Locate every cell, classifying each as a parasitized red blood cell, an uninfected red blood cell, or a white blood cell.
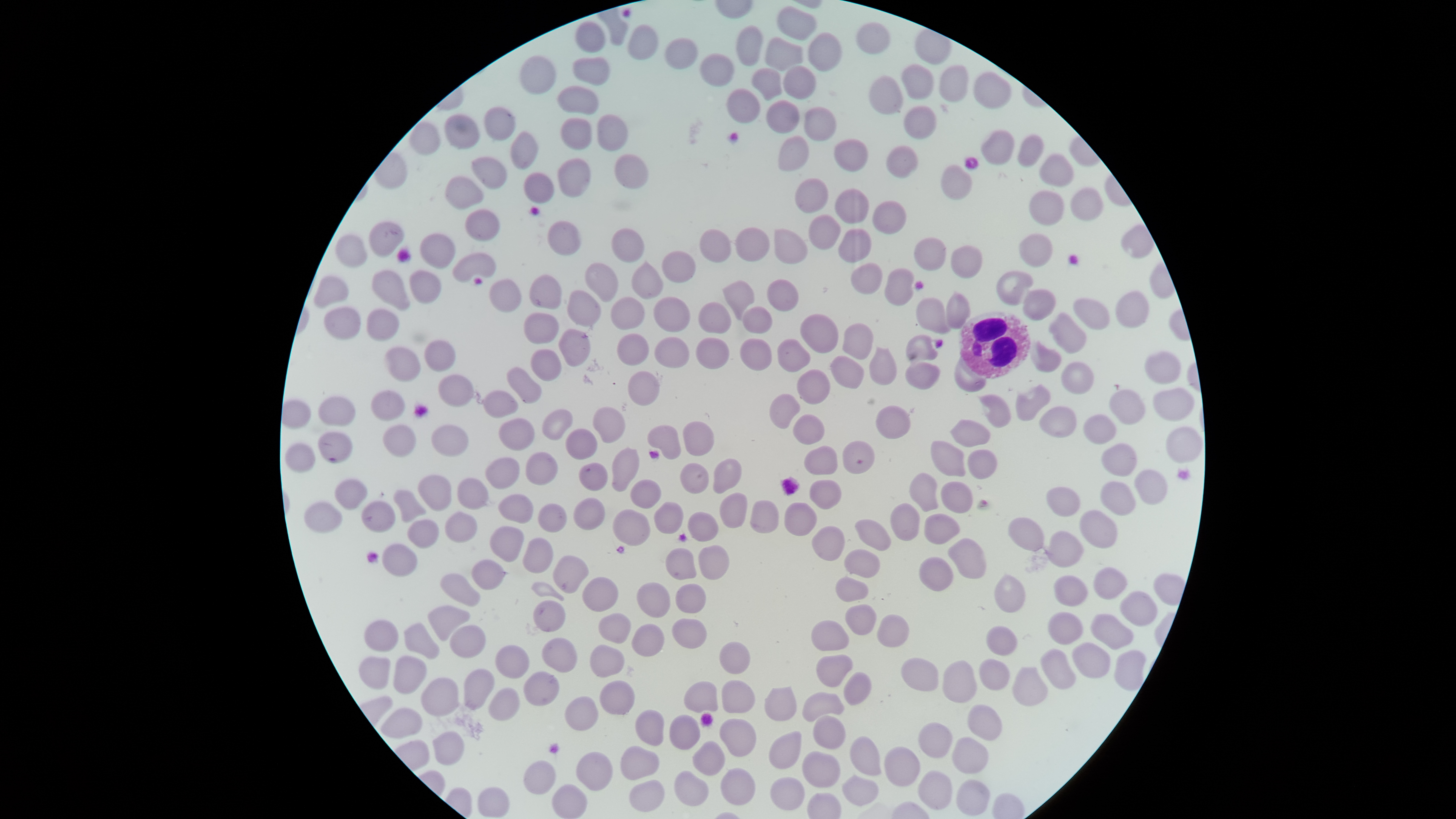

No parasitized red blood cells identified.
Approximate bounding boxes as {left, top, right, bottom} in pixels.
Uninfected red blood cells: {776, 6, 816, 40}, {574, 20, 605, 54}, {856, 22, 890, 55}, {627, 24, 658, 61}, {736, 24, 762, 66}, {808, 32, 842, 73}, {664, 37, 698, 70}, {765, 37, 803, 71}, {699, 53, 734, 88}, {520, 56, 556, 95}, {572, 56, 610, 86}, {901, 64, 934, 100}, {783, 65, 817, 99}, {939, 65, 969, 103}, {751, 68, 783, 101}, {973, 71, 1012, 109}, {868, 75, 904, 116}, {557, 86, 599, 115}, {726, 89, 760, 124}, {766, 99, 800, 134}, {903, 105, 936, 139}, {483, 106, 516, 141}, {803, 106, 837, 142}, {443, 114, 480, 150}, {597, 114, 628, 152}, {560, 118, 592, 150}, {409, 121, 440, 155}, {980, 129, 1015, 166}, {510, 130, 538, 170}, {1017, 134, 1044, 167}, {778, 135, 809, 172}, {833, 139, 869, 173}, {886, 145, 919, 179}, {1038, 153, 1075, 187}, {614, 154, 650, 189}, {471, 156, 507, 190}, {557, 159, 591, 197}, {940, 164, 973, 201}, {523, 173, 554, 204}, {445, 176, 483, 209}, {794, 178, 829, 213}, {1069, 187, 1103, 221}, {835, 188, 869, 224}, {1028, 190, 1065, 226}, {872, 200, 906, 234}, {464, 209, 500, 242}, {808, 214, 841, 250}, {547, 220, 581, 256}, {368, 221, 405, 258}, {735, 227, 770, 261}, {611, 228, 645, 263}, {838, 228, 871, 263}, {699, 229, 731, 262}, {774, 229, 808, 265}, {1018, 233, 1054, 267}, {335, 234, 367, 268}, {419, 234, 456, 269}, {913, 237, 947, 271}, {950, 245, 982, 279}, {661, 250, 697, 283}, {451, 252, 497, 283}, {630, 260, 664, 299}, {585, 263, 619, 303}, {851, 263, 883, 295}, {884, 268, 915, 306}, {371, 269, 411, 311}, {409, 270, 441, 304}, {996, 270, 1033, 307}, {529, 275, 563, 310}, {313, 276, 348, 309}, {766, 279, 799, 312}, {722, 280, 754, 320}, {1022, 288, 1056, 322}, {566, 290, 601, 328}, {1115, 290, 1149, 328}, {945, 292, 970, 330}, {610, 297, 645, 330}, {653, 297, 690, 333}, {915, 297, 950, 335}, {1073, 297, 1110, 330}, {698, 301, 731, 334}, {323, 306, 360, 340}, {742, 306, 773, 333}, {366, 308, 400, 341}, {1048, 312, 1087, 354}, {523, 313, 560, 345}, {800, 314, 838, 354}, {842, 323, 874, 360}, {558, 329, 591, 367}, {617, 334, 649, 366}, {905, 334, 938, 364}, {654, 337, 690, 368}, {695, 337, 729, 369}, {740, 338, 772, 371}, {422, 339, 456, 372}, {777, 339, 811, 373}, {1029, 339, 1062, 373}, {384, 346, 421, 381}, {869, 346, 896, 385}, {530, 349, 562, 381}, {1144, 351, 1181, 385}, {829, 355, 865, 389}, {905, 361, 941, 390}, {1061, 361, 1094, 395}, {506, 366, 542, 404}, {796, 369, 830, 405}, {627, 371, 660, 406}, {437, 374, 474, 407}, {1015, 383, 1051, 422}, {1152, 387, 1195, 422}, {1108, 389, 1146, 425}, {371, 390, 405, 422}, {483, 390, 518, 419}, {769, 393, 801, 430}, {978, 395, 1012, 429}, {317, 396, 356, 427}, {875, 405, 911, 439}, {593, 406, 626, 443}, {1038, 406, 1077, 439}, {541, 408, 573, 441}, {792, 414, 825, 445}, {1083, 414, 1116, 445}, {499, 418, 534, 452}, {949, 419, 991, 448}, {682, 421, 715, 457}, {383, 424, 416, 457}, {430, 424, 469, 457}, {647, 425, 681, 460}, {1165, 426, 1202, 464}, {565, 429, 598, 460}, {317, 432, 353, 464}, {842, 441, 875, 474}, {930, 441, 965, 477}, {1102, 442, 1137, 477}, {284, 443, 316, 473}, {804, 445, 838, 476}, {611, 447, 640, 492}, {967, 449, 997, 480}, {525, 452, 558, 486}, {485, 457, 520, 489}, {713, 458, 743, 494}, {578, 461, 608, 492}, {679, 463, 709, 494}, {1133, 469, 1167, 505}, {909, 473, 939, 512}, {417, 475, 452, 511}, {457, 478, 490, 510}, {334, 479, 368, 510}, {630, 480, 662, 509}, {809, 480, 842, 510}, {940, 481, 973, 513}, {1100, 481, 1136, 516}, {1045, 487, 1080, 517}, {393, 489, 426, 523}, {719, 492, 747, 529}, {498, 494, 534, 524}, {573, 497, 605, 530}, {749, 500, 779, 534}, {361, 501, 396, 533}, {654, 501, 684, 534}, {304, 502, 342, 533}, {784, 502, 818, 537}, {890, 502, 920, 542}, {538, 503, 567, 533}, {612, 509, 651, 546}, {1079, 509, 1118, 549}, {687, 511, 719, 542}, {445, 512, 478, 543}, {924, 513, 961, 545}, {1008, 517, 1044, 552}, {407, 519, 440, 549}, {855, 519, 892, 551}, {489, 526, 525, 562}, {811, 526, 845, 562}, {1047, 530, 1084, 568}, {948, 537, 987, 579}, {522, 538, 553, 574}, {381, 544, 417, 577}, {698, 544, 729, 580}, {665, 547, 697, 580}, {843, 548, 880, 579}, {552, 554, 590, 594}, {919, 556, 953, 591}, {471, 559, 505, 590}, {1093, 567, 1128, 600}, {439, 574, 480, 606}, {993, 574, 1025, 613}, {1053, 575, 1088, 606}, {581, 577, 619, 612}, {635, 582, 671, 618}, {675, 583, 706, 614}, {1119, 590, 1158, 627}, {533, 599, 566, 632}, {845, 604, 877, 636}, {428, 605, 470, 640}, {598, 612, 631, 644}, {1047, 612, 1083, 644}, {877, 614, 909, 648}, {1089, 614, 1134, 650}, {672, 618, 707, 649}, {364, 620, 398, 652}, {810, 620, 849, 651}, {631, 622, 665, 657}, {404, 623, 439, 659}, {450, 625, 486, 658}, {985, 626, 1018, 655}, {542, 637, 577, 673}, {718, 641, 751, 674}, {1072, 642, 1111, 679}, {494, 645, 530, 679}, {590, 645, 624, 678}, {1040, 648, 1076, 690}, {1114, 650, 1146, 691}, {815, 654, 853, 687}, {394, 655, 427, 694}, {358, 657, 391, 689}, {900, 658, 939, 692}, {979, 658, 1009, 691}, {942, 660, 977, 703}, {1012, 667, 1047, 706}, {463, 668, 495, 710}, {523, 671, 559, 707}, {843, 672, 872, 706}, {422, 678, 459, 717}, {721, 680, 755, 713}, {599, 681, 635, 715}, {683, 681, 718, 712}, {764, 686, 796, 722}, {488, 687, 520, 721}, {802, 692, 844, 721}, {565, 696, 599, 731}, {967, 704, 1003, 740}, {381, 708, 422, 738}, {634, 710, 664, 745}, {669, 715, 700, 750}, {812, 716, 846, 749}, {719, 718, 757, 757}, {917, 722, 952, 759}, {432, 730, 464, 765}, {768, 731, 802, 769}, {849, 735, 882, 775}, {952, 736, 989, 774}, {693, 741, 725, 775}, {620, 746, 660, 780}, {884, 746, 920, 787}, {801, 751, 840, 788}, {576, 752, 613, 791}, {524, 761, 556, 795}, {720, 768, 755, 805}, {918, 770, 952, 811}, {674, 771, 709, 806}, {842, 774, 878, 807}, {770, 777, 805, 810}, {956, 779, 990, 816}, {629, 780, 665, 812}, {552, 785, 588, 818}, {477, 787, 510, 817}.
White blood cells: {957, 310, 1031, 379}.

Summary:
  - Capture: smartphone photograph through the microscope eyepiece
  - Visible region: circular
  - Stain: Giemsa
  - Image size: 1456×819 pixels
  - Preparation: thin blood film
  - Field of view: single